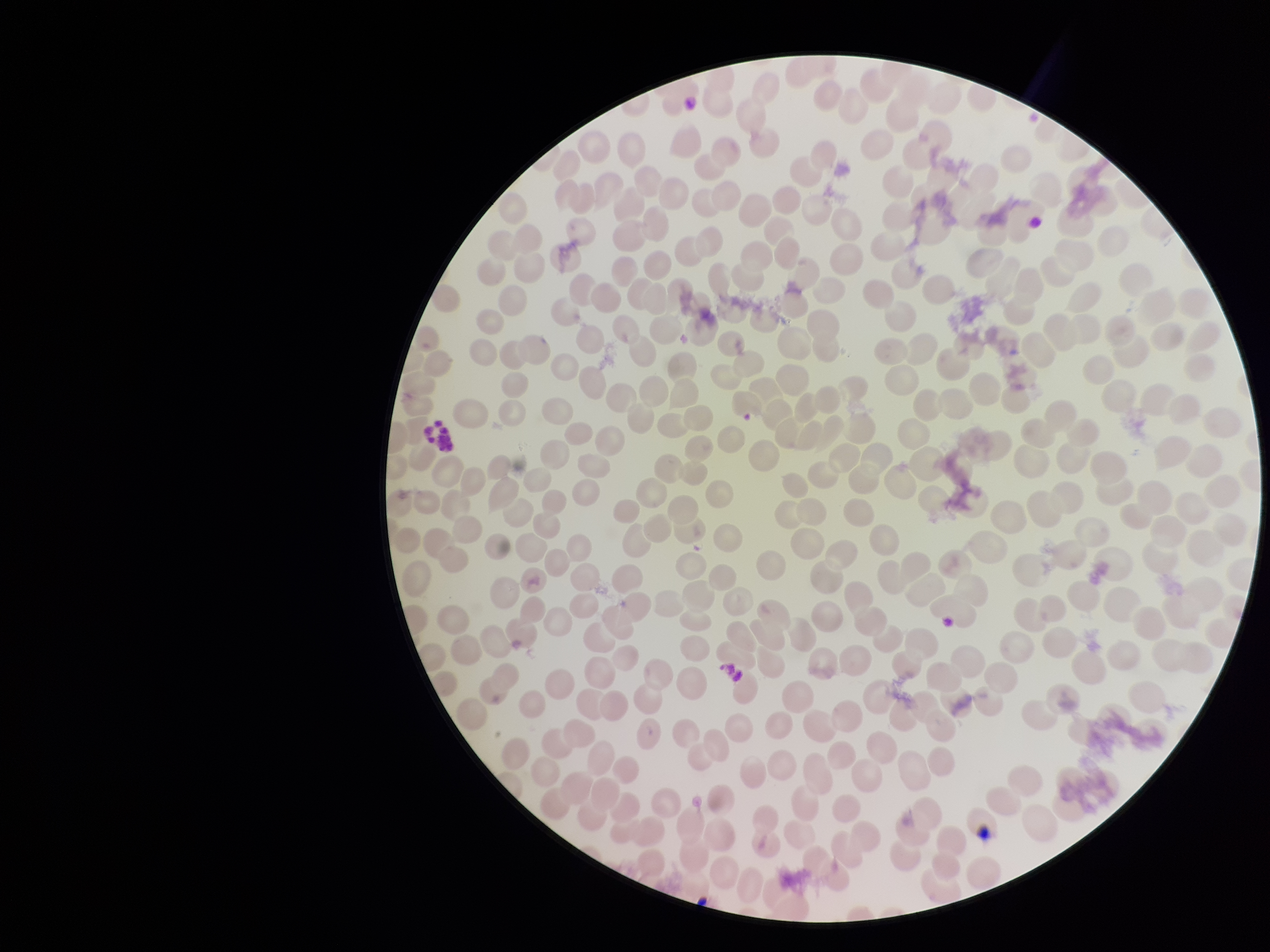

{
  "field_of_view": "single",
  "patient_malaria_status": "negative",
  "capture": "smartphone photograph through the microscope eyepiece",
  "parasitized_red_blood_cell_count": 0,
  "parasitized_red_blood_cells": "none seen",
  "preparation": "thin blood smear",
  "image_size": "1270×952 pixels",
  "red_blood_cell_count": 313,
  "stain": "Giemsa"
}